Locate every Plasmodium falciparum-infected red blood cell.
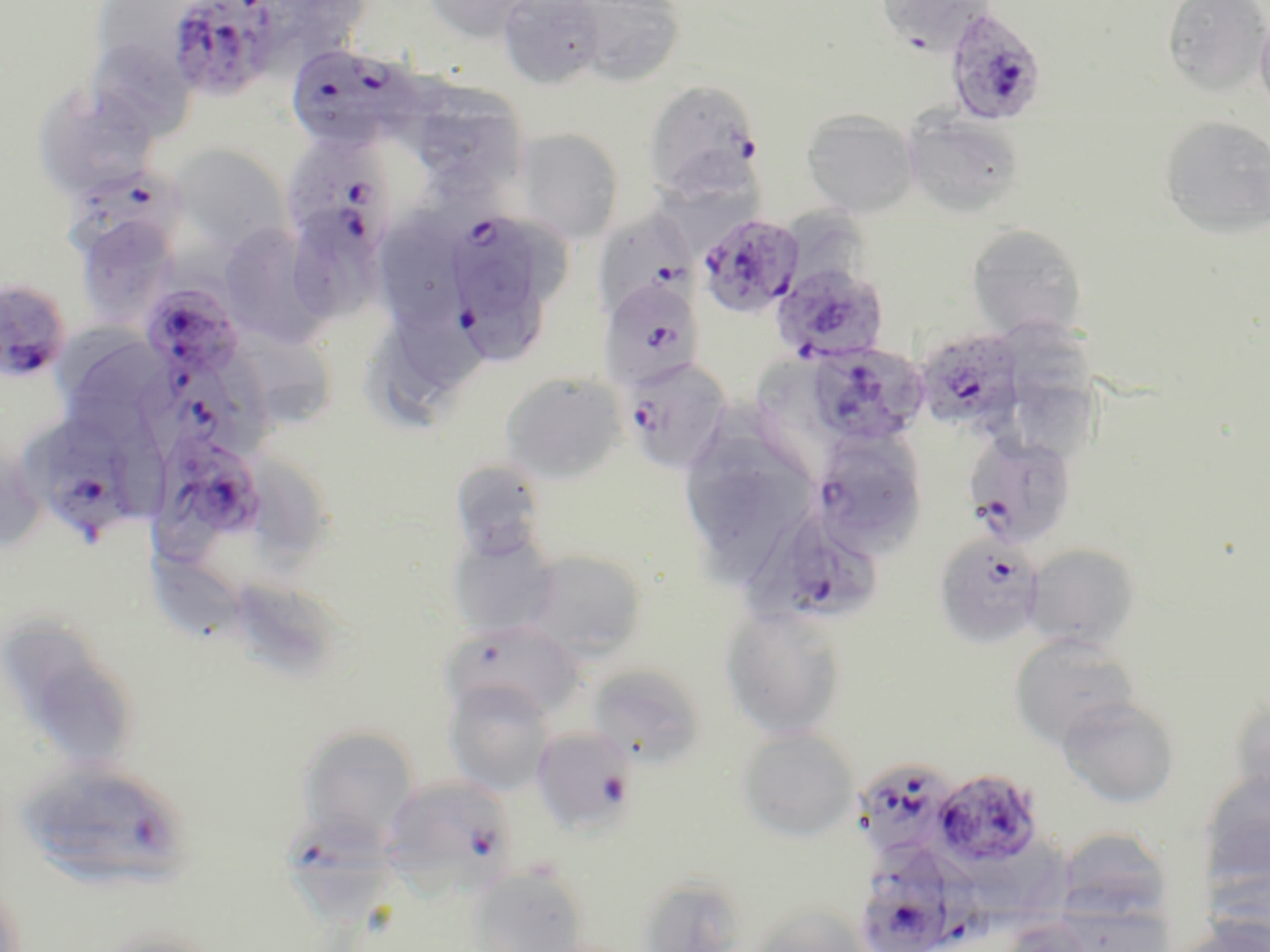

Approximate bounding boxes as (x1, y1, x2, y2) in pixels.
Plasmodium falciparum-infected red blood cells (subset): (166, 0, 279, 101), (942, 6, 1048, 127), (285, 43, 421, 152), (642, 80, 763, 199), (285, 136, 393, 260), (53, 167, 189, 270), (600, 212, 695, 314), (696, 213, 804, 318), (454, 215, 539, 317), (456, 260, 547, 369), (777, 269, 892, 367), (598, 277, 705, 391), (0, 278, 71, 385), (140, 281, 247, 384), (914, 328, 1025, 436), (803, 342, 926, 449), (621, 356, 733, 473), (161, 373, 249, 463), (32, 426, 135, 533), (810, 429, 927, 554), (158, 432, 265, 542), (963, 432, 1077, 549), (760, 505, 886, 630), (532, 726, 637, 834), (851, 758, 961, 867), (14, 760, 195, 891), (931, 768, 1045, 869), (381, 774, 517, 894), (289, 813, 400, 923), (977, 851, 1066, 926), (913, 853, 990, 947), (865, 855, 952, 952).

Uninfected red blood cell locations (subset): (257, 0, 358, 75), (421, 0, 544, 42), (497, 0, 607, 90), (874, 0, 997, 53), (1161, 0, 1270, 96), (100, 1, 193, 59), (570, 1, 686, 86), (1254, 7, 1270, 123), (84, 37, 198, 142), (32, 85, 159, 202), (418, 88, 526, 194), (800, 108, 919, 217), (902, 111, 1026, 219), (1159, 116, 1270, 239), (514, 128, 626, 245), (168, 144, 292, 254), (657, 151, 765, 258), (788, 206, 870, 288), (297, 212, 385, 322), (73, 213, 181, 328), (216, 221, 333, 346), (965, 223, 1088, 342), (383, 227, 465, 324), (389, 288, 484, 396), (1005, 323, 1095, 408), (369, 325, 461, 431), (54, 328, 173, 443), (241, 335, 332, 427), (752, 357, 823, 435), (499, 371, 627, 485), (1007, 383, 1105, 465), (114, 426, 171, 518), (257, 458, 324, 571), (449, 460, 550, 562), (446, 530, 563, 641), (1023, 543, 1141, 652), (520, 548, 649, 661), (147, 549, 244, 640), (237, 578, 334, 668), (720, 604, 848, 741), (5, 616, 104, 702), (444, 621, 582, 721), (1008, 633, 1140, 750), (585, 663, 705, 770), (33, 667, 128, 757), (443, 678, 556, 795), (1056, 694, 1181, 808), (1228, 696, 1270, 810), (298, 725, 420, 842), (736, 726, 861, 842), (1199, 770, 1270, 891), (1054, 827, 1175, 928), (468, 865, 588, 951), (1205, 867, 1270, 949), (634, 871, 748, 952), (0, 873, 28, 952), (1052, 898, 1173, 952), (747, 905, 874, 952), (1166, 918, 1270, 952), (997, 919, 1094, 952), (91, 926, 225, 952). Slide-level diagnosis: Plasmodium falciparum. Thin blood smear. Light microscopy. Image is 1270×952 pixels. Single field of view. May-Grünwald-Giemsa-stained preparation. 1000x magnification.